Classify this cell by malaria status.
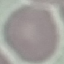

Uninfected.

Thin blood smear. Acquired by smartphone through the microscope eyepiece. Giemsa stain. Cell patch, automatically extracted from a larger field of view and resized to 64 × 64 pixels.